Report the malaria status of this cell.
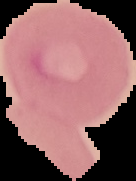
Uninfected.

Summary:
  - Image size: 136×181 pixels
  - Preparation: thin blood film
  - Image type: segmented cell region with the area outside set to black